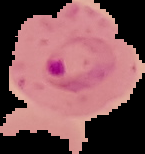
image_size: 145×154 pixels
preparation: thin blood smear
image_type: segmented cell region on a black background
malaria_status: parasitized